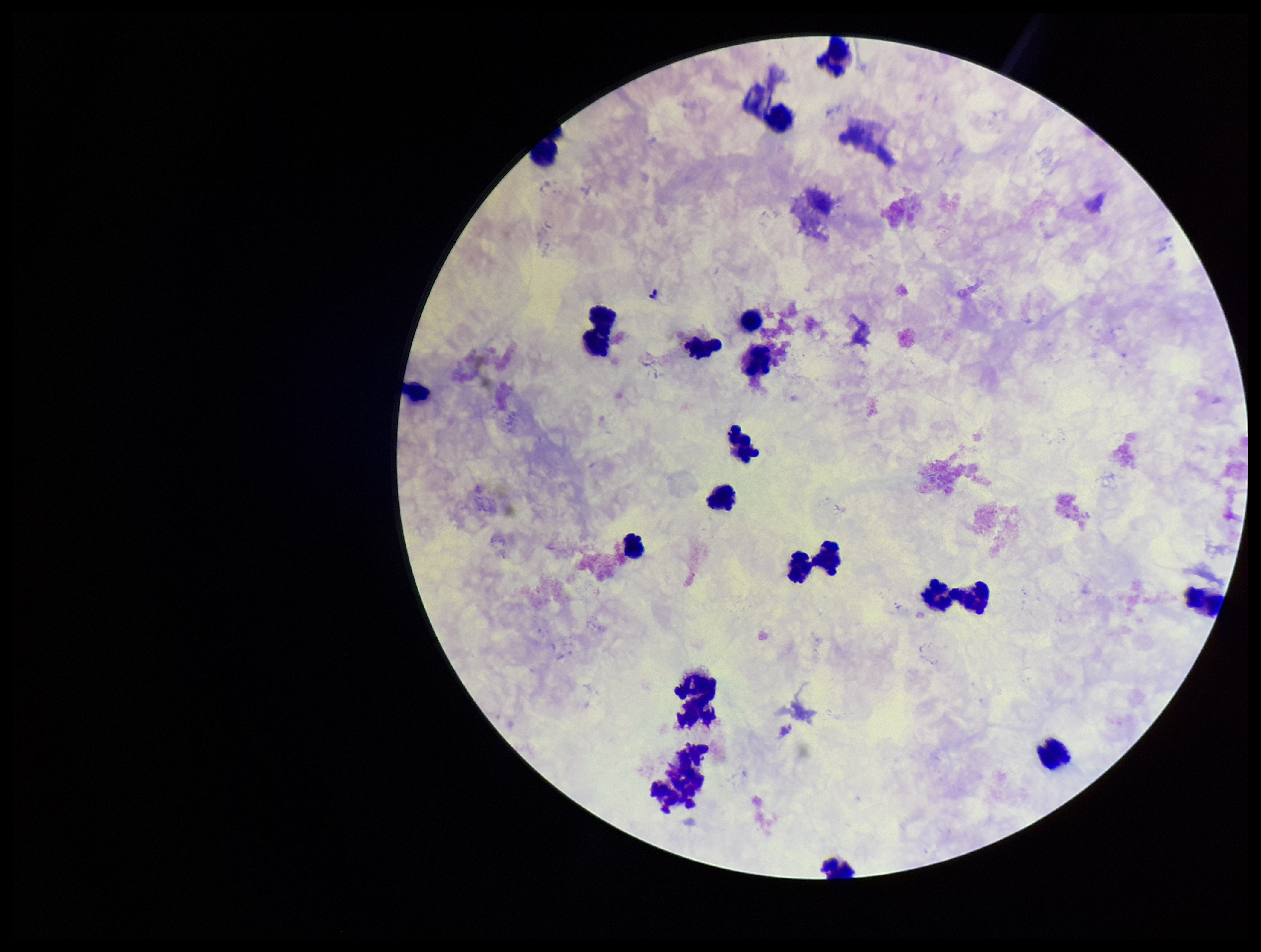

Summary:
  - Image size: 1261×952 pixels
  - Field of view: one from this slide
  - Parasite count: 0
  - Plasmodium parasites: none detected
  - Preparation: thick
  - Stain: Giemsa
  - Leukocyte count: 19
  - Patient malaria status: negative
  - Capture: smartphone photograph through the microscope eyepiece